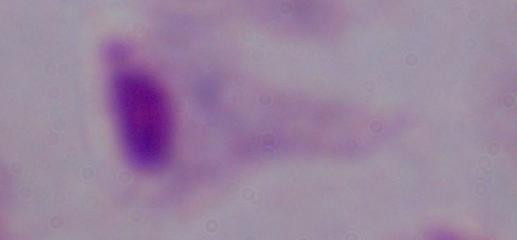

Micrograph. A trichomonad is shown. 1000x magnification.